Locate every uninfected red blood cell.
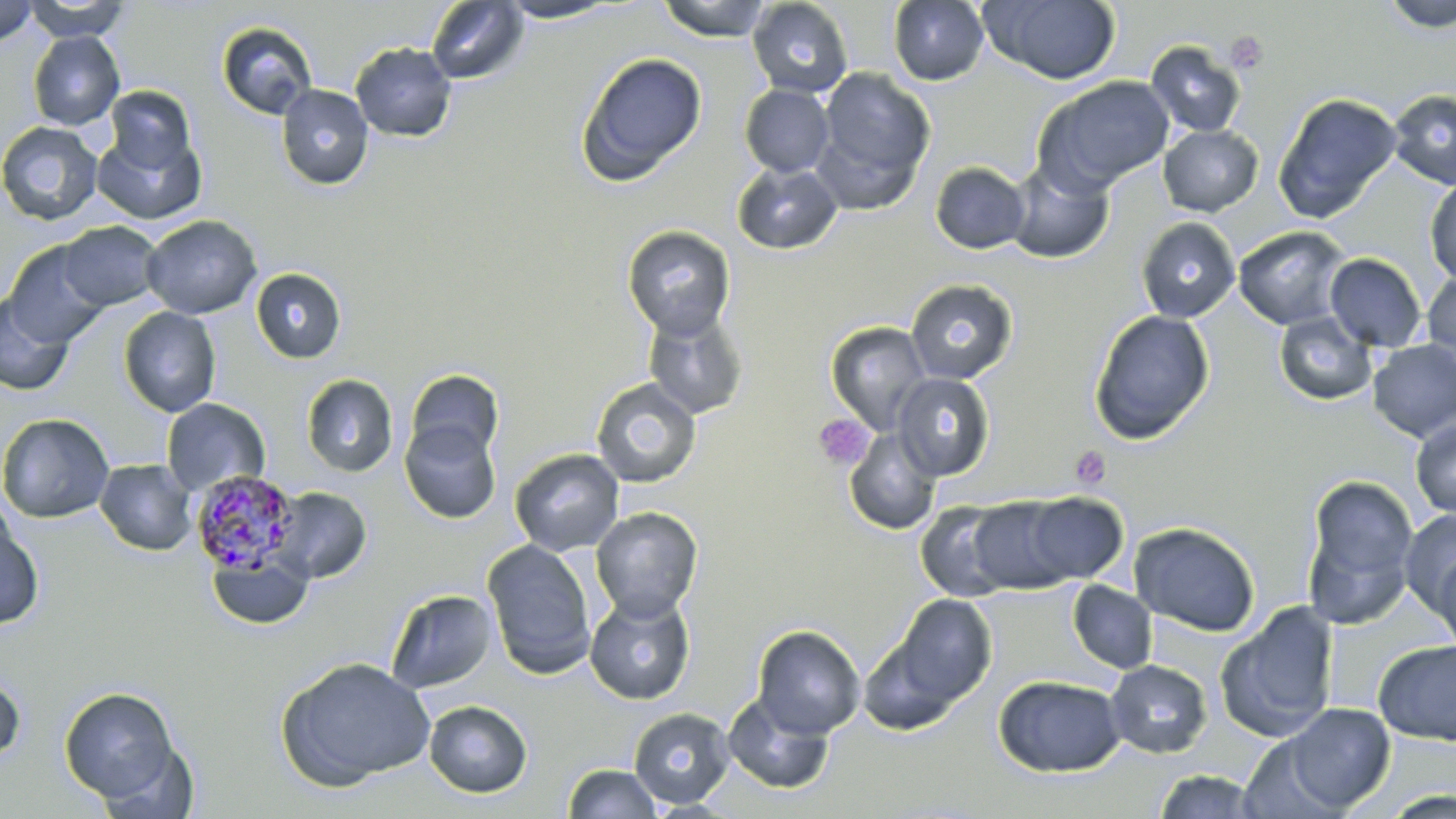

Approximate bounding boxes as (x1, y1, x2, y2) in pixels.
Uninfected red blood cells: (23, 0, 133, 41), (656, 0, 772, 42), (747, 0, 854, 99), (888, 0, 989, 86), (982, 0, 1122, 85), (1381, 0, 1456, 33), (0, 1, 38, 46), (425, 1, 529, 85), (496, 1, 625, 24), (216, 21, 318, 120), (28, 31, 125, 130), (1145, 40, 1246, 138), (350, 42, 457, 143), (575, 52, 707, 186), (814, 66, 935, 205), (1033, 76, 1175, 194), (276, 84, 374, 191), (740, 84, 834, 177), (105, 85, 195, 173), (1388, 89, 1456, 190), (1272, 92, 1402, 223), (0, 121, 103, 226), (1158, 124, 1264, 217), (92, 128, 206, 224), (1006, 159, 1114, 264), (732, 161, 842, 255), (930, 162, 1030, 254), (1425, 177, 1456, 285), (141, 215, 262, 319), (1135, 216, 1240, 323), (58, 221, 163, 311), (622, 225, 735, 339), (1233, 225, 1352, 330), (2, 241, 110, 348), (1324, 253, 1426, 352), (251, 268, 347, 363), (1423, 269, 1456, 368), (905, 279, 1018, 384), (0, 292, 75, 396), (118, 307, 221, 417), (643, 309, 748, 421), (1088, 309, 1214, 444), (1273, 312, 1377, 407), (824, 322, 932, 434), (1368, 340, 1456, 442), (403, 368, 504, 466), (892, 372, 995, 481), (301, 374, 398, 477), (591, 377, 702, 488), (162, 398, 270, 496), (0, 412, 115, 523), (1410, 418, 1456, 519), (400, 419, 502, 524), (844, 429, 942, 535), (509, 448, 625, 556), (95, 459, 197, 555), (1302, 472, 1420, 628), (268, 486, 372, 584), (1020, 491, 1128, 585), (967, 496, 1079, 593), (915, 501, 1017, 602), (591, 507, 703, 621), (1399, 509, 1456, 616), (0, 515, 44, 630), (1129, 521, 1261, 637), (482, 539, 598, 679), (1432, 546, 1456, 659), (206, 550, 314, 631), (1067, 580, 1158, 674), (385, 589, 498, 694), (585, 591, 695, 705), (892, 594, 998, 705), (1217, 601, 1340, 743), (752, 625, 866, 739), (858, 637, 964, 736), (1373, 639, 1456, 746), (275, 657, 436, 790), (1106, 659, 1212, 759), (0, 672, 25, 766), (992, 674, 1126, 777), (59, 686, 181, 805), (722, 692, 834, 795), (423, 700, 532, 798), (1279, 703, 1395, 812), (628, 707, 735, 809), (1239, 734, 1346, 819), (94, 738, 203, 817), (562, 763, 662, 819), (1152, 769, 1266, 819), (1380, 790, 1456, 819).

slide-level diagnosis = Plasmodium malariae
stain = May-Grünwald-Giemsa
Plasmodium malariae-infected red blood cell locations = approximate bounding boxes as (x1, y1, x2, y2) in pixels: (190, 470, 301, 575)
modality = optical microscopy
field of view = single
image size = 1456×819 pixels
platelet locations = approximate bounding boxes as (x1, y1, x2, y2) in pixels: (1225, 31, 1268, 75), (812, 414, 874, 471), (1070, 446, 1111, 490)
preparation = thin blood film
magnification = 1000x